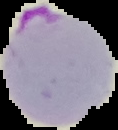
Summary:
  - Preparation: thin blood film
  - Image size: 118×130 pixels
  - Result: Plasmodium parasites detected
  - Image type: segmented cell region on a black background